State the blood parasite species.
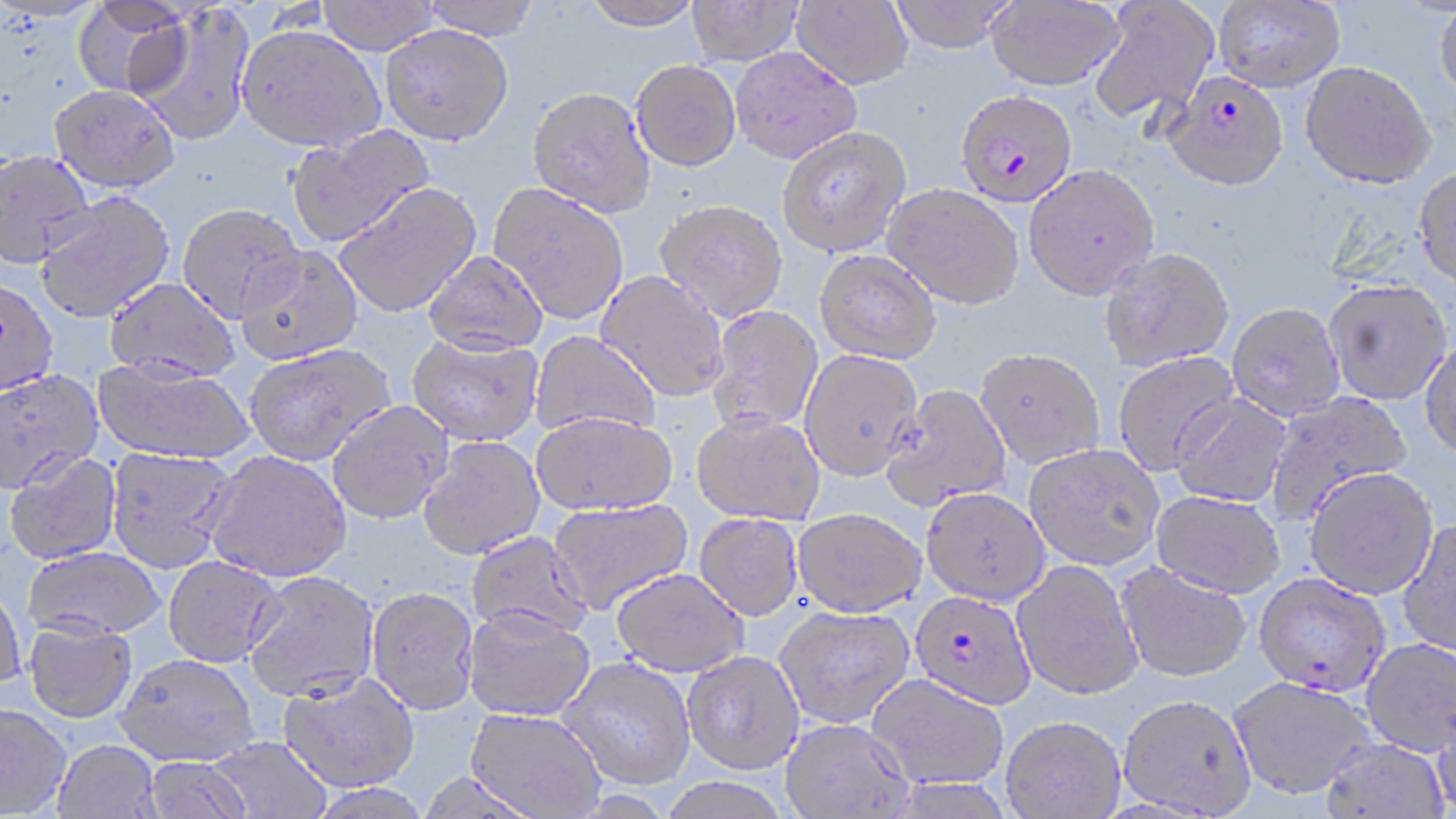
Plasmodium falciparum.

field of view = single
image size = 1456×819 pixels
stain = May-Grünwald-Giemsa
modality = light microscopy
Plasmodium falciparum-infected red blood cell locations = approximate bounding boxes as (x1, y1, x2, y2) in pixels: (1163, 72, 1290, 192), (954, 89, 1078, 207), (1253, 573, 1390, 696), (909, 590, 1037, 709)
preparation = thin blood smear
uninfected red blood cell locations = approximate bounding boxes as (x1, y1, x2, y2) in pixels: (315, 0, 442, 55), (417, 0, 545, 40), (580, 0, 705, 30), (886, 0, 1019, 53), (985, 0, 1125, 90), (1214, 0, 1344, 92), (72, 1, 191, 99), (685, 1, 803, 65), (792, 1, 913, 89), (1087, 1, 1220, 126), (1434, 3, 1456, 104), (132, 5, 256, 146), (380, 24, 515, 146), (236, 25, 386, 152), (730, 47, 862, 163), (631, 59, 741, 171), (1300, 60, 1436, 188), (48, 84, 181, 193), (527, 85, 656, 218), (285, 125, 434, 248), (777, 125, 911, 257), (0, 148, 97, 269), (1024, 163, 1160, 300), (1413, 166, 1456, 289), (334, 183, 482, 318), (489, 183, 629, 324), (882, 184, 1024, 309), (34, 191, 175, 324), (656, 198, 790, 322), (178, 203, 304, 323), (236, 246, 363, 366), (1099, 247, 1235, 371), (422, 250, 548, 357), (814, 250, 941, 365), (596, 270, 730, 402), (104, 277, 241, 383), (0, 278, 58, 398), (1322, 278, 1453, 404), (1227, 302, 1345, 421), (706, 305, 823, 435), (530, 331, 660, 438), (406, 332, 545, 446), (1420, 338, 1456, 459), (244, 344, 396, 466), (975, 347, 1105, 467), (799, 350, 922, 481), (1113, 352, 1239, 475), (92, 357, 253, 465), (0, 369, 104, 494), (880, 384, 1013, 510), (1263, 390, 1412, 525), (1171, 393, 1292, 507), (327, 401, 453, 525), (531, 411, 678, 516), (691, 411, 826, 525), (418, 436, 546, 560), (1024, 443, 1165, 570), (105, 447, 240, 573), (4, 451, 122, 565), (204, 451, 351, 583), (1303, 467, 1439, 599), (921, 487, 1050, 605), (1151, 490, 1285, 597), (547, 498, 694, 615), (791, 507, 927, 616), (694, 513, 803, 620), (1397, 518, 1456, 657), (465, 531, 593, 640), (23, 547, 166, 641), (162, 556, 284, 668), (1012, 560, 1143, 700), (1116, 563, 1251, 682), (610, 568, 749, 677), (243, 570, 380, 703), (0, 580, 27, 697), (365, 586, 480, 715), (773, 604, 915, 727), (462, 605, 596, 722), (23, 619, 138, 724), (1360, 637, 1456, 757), (682, 650, 805, 774), (115, 653, 259, 766), (557, 656, 696, 789), (278, 671, 420, 792), (866, 673, 1009, 789), (1228, 675, 1377, 800), (1117, 693, 1257, 817), (0, 705, 72, 817), (1431, 705, 1456, 818), (466, 707, 607, 818), (1000, 715, 1125, 818), (780, 717, 913, 818), (204, 736, 331, 819), (1321, 738, 1449, 819), (53, 740, 163, 819), (141, 755, 256, 818), (414, 770, 547, 819), (655, 777, 794, 819)
magnification = 1000x